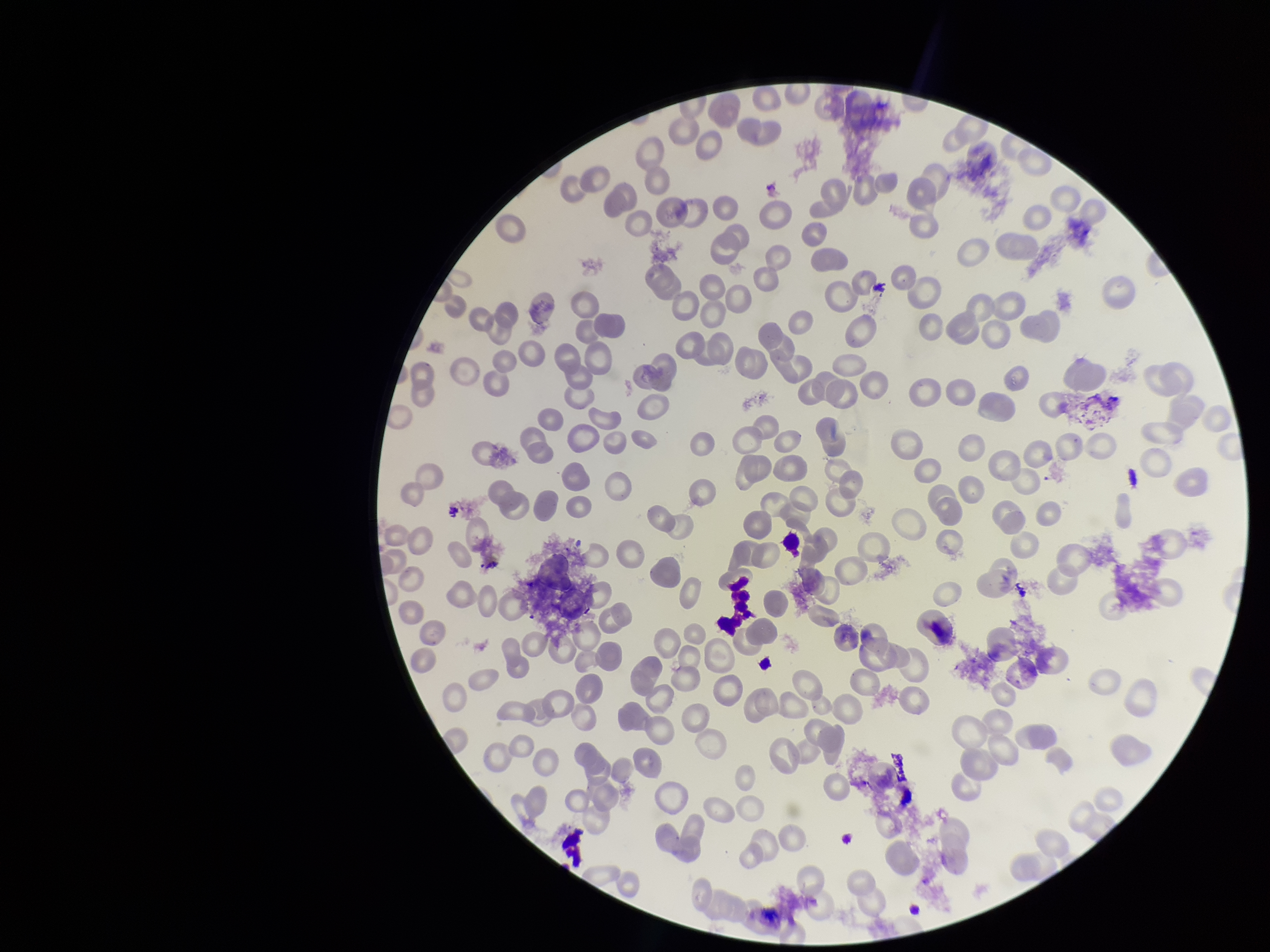
{
  "parasitized_red_blood_cell_count": 0,
  "preparation": "thin smear",
  "parasitized_red_blood_cells": "none identified",
  "capture": "smartphone photograph through the microscope eyepiece",
  "field_of_view": "one from this slide",
  "patient_malaria_status": "negative",
  "image_size": "1270×952 pixels",
  "red_blood_cell_count": 188,
  "stain": "Giemsa"
}